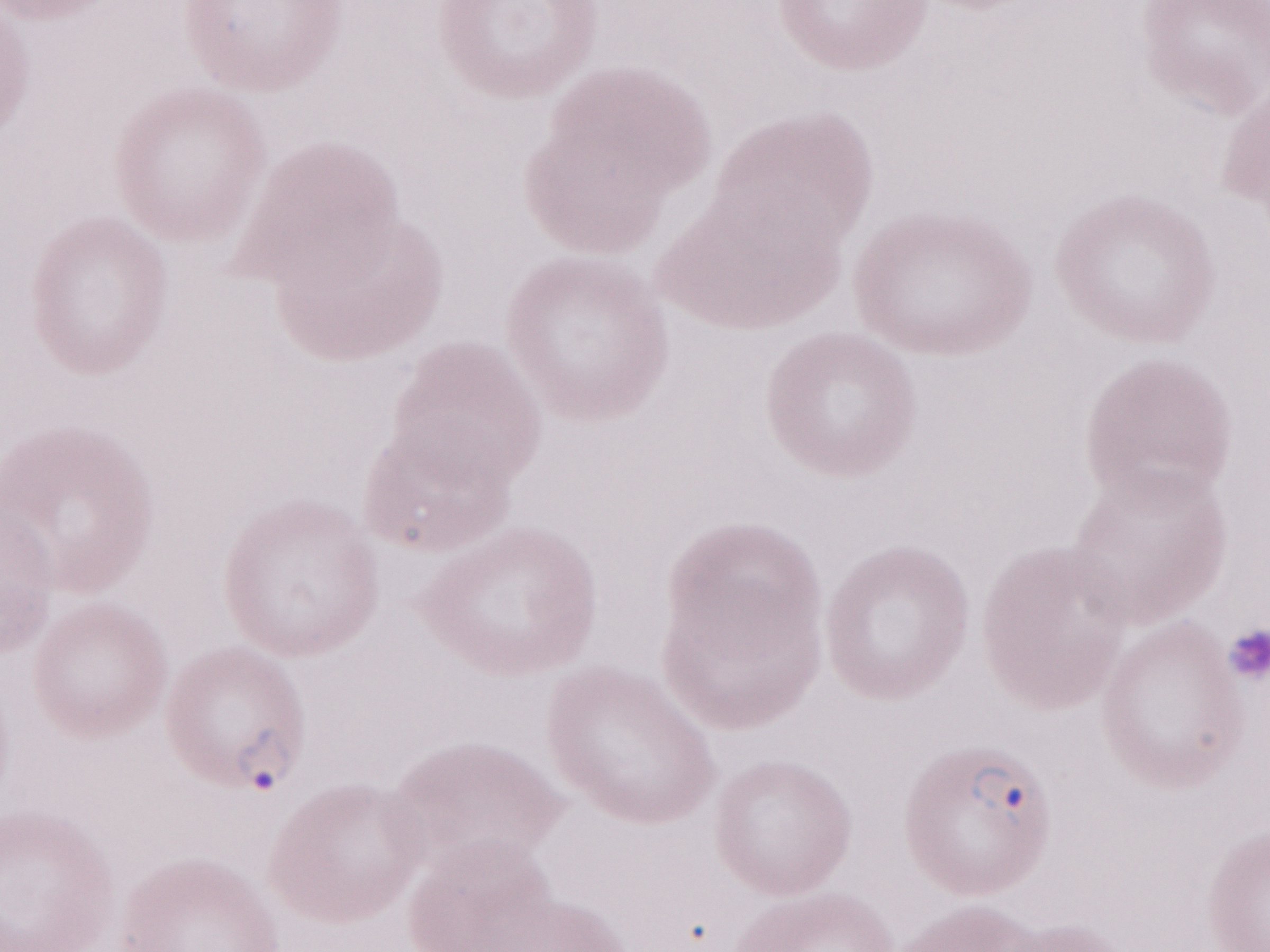
Olympus BX43 microscope, Olympus DP73 camera. Thin peripheral-blood smear. May-Grünwald-Giemsa-stained preparation. Magnification: 1,000x. Single field of view. Patient-level malaria diagnosis: positive. Image is 1270×952 pixels.